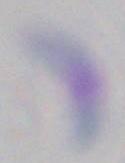

identification = Toxoplasma gondii
magnification = 1000x
modality = micrograph